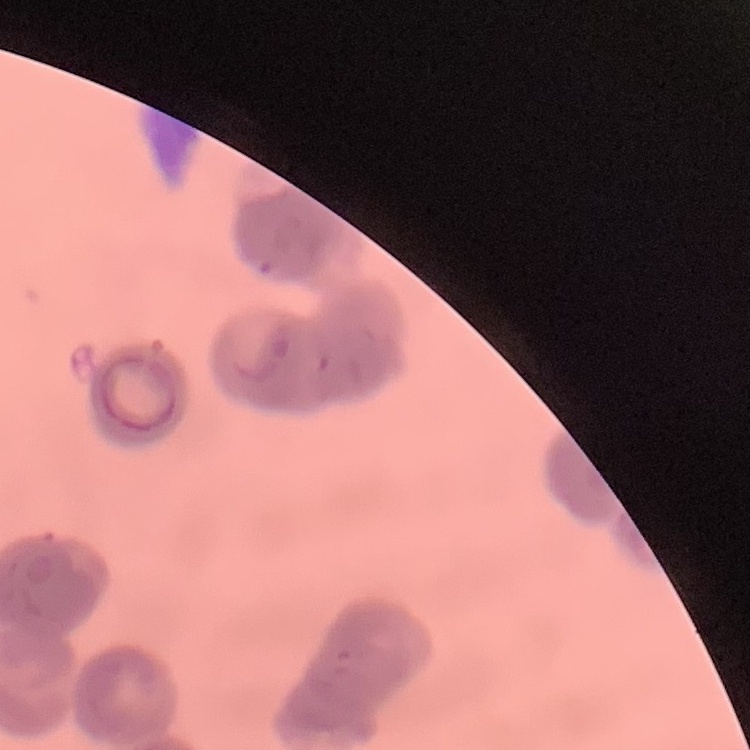 The erythrocytes show rouleaux formation. Field's or Giemsa stain. Square crop of a larger photomicrograph. Thin peripheral smear.